Name the parasite shown.
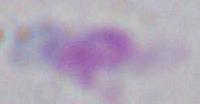

Toxoplasma gondii.

Photomicrograph. 1000x magnification.